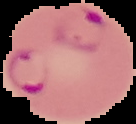

{
  "image_size": "136×124 pixels",
  "malaria_status": "parasitized",
  "preparation": "thin blood smear",
  "image_type": "segmented cell region on a black background"
}